Report the malaria status of this cell.
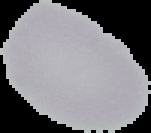

It is uninfected.

{
  "preparation": "thin blood film",
  "image_type": "segmented cell region with the area outside set to black",
  "image_size": "151×133 pixels"
}